Identify the parasite.
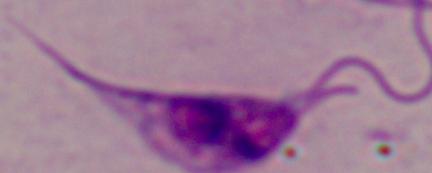

This is Leishmania.

modality: photomicrograph
magnification: 1000x